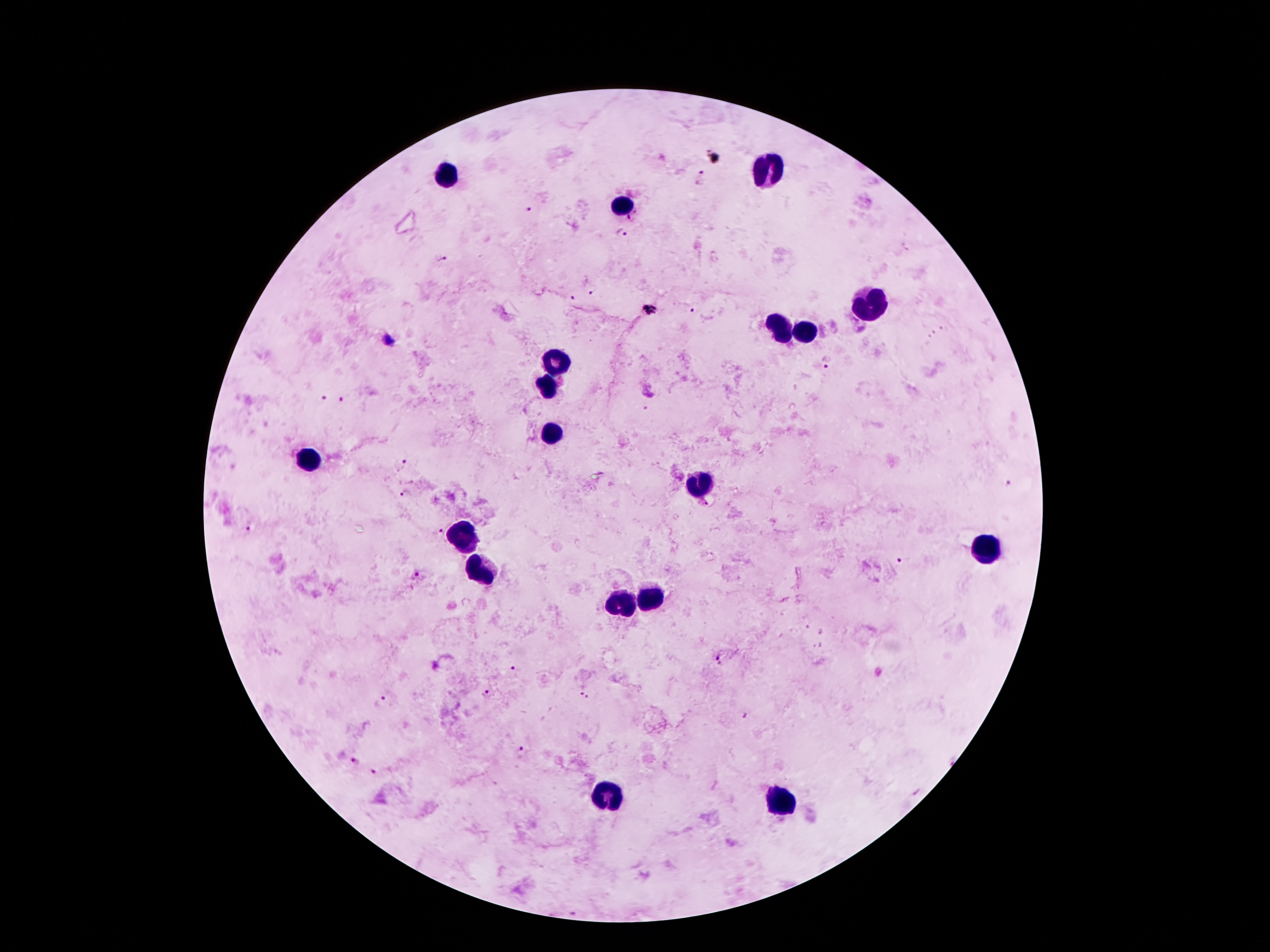
Approximate centers as (x, y) in pixels.
Summary:
  - Malaria parasite locations: (702, 176), (532, 209), (632, 216), (621, 233), (440, 258), (591, 293), (574, 299), (691, 310), (829, 363), (322, 397), (341, 400), (399, 464), (404, 494), (247, 530), (439, 532), (898, 560), (416, 576), (716, 662), (512, 668), (582, 693), (488, 694), (380, 702), (520, 750), (355, 763), (374, 773)
  - Leukocyte locations: (766, 169), (452, 176), (622, 205), (870, 304), (781, 326), (806, 333), (558, 360), (547, 386), (551, 435), (308, 461), (704, 483), (461, 539), (989, 545), (481, 574), (649, 595), (622, 604), (609, 794), (781, 801)
  - Image size: 1270×952 pixels
  - Field of view: one from this slide
  - Magnification: 100x
  - Preparation: thick peripheral-blood smear
  - Patient malaria status: infected with Plasmodium falciparum
  - Stain: Giemsa
  - Capture: smartphone through the microscope eyepiece